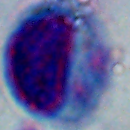

magnification: 1000x
identification: leukocyte
modality: photomicrograph